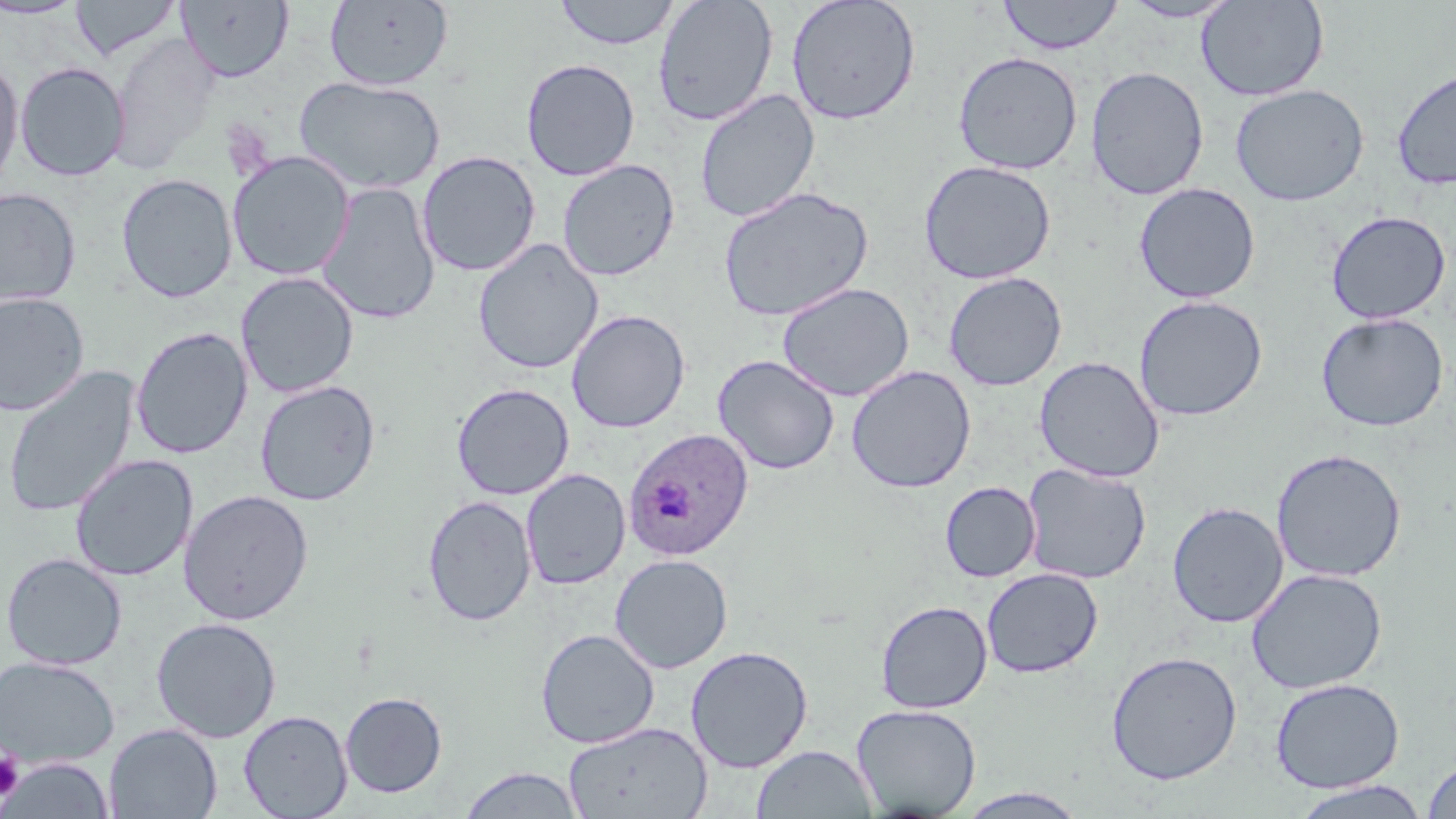

slide-level diagnosis = Plasmodium ovale
preparation = thin blood smear
magnification = 1000x
platelet locations = approximate bounding boxes as (x1,y1)-(x2,y2) corner pairs in pixels: (0,751)-(24,801)
field of view = one of a larger specimen
image size = 1456×819 pixels
modality = light microscopy
uninfected red blood cell locations = approximate bounding boxes as (x1,y1)-(x2,y2) corner pairs in pixels: (71,0)-(181,61), (324,0)-(454,91), (553,0)-(681,50), (652,0)-(779,127), (786,0)-(921,126), (996,0)-(1125,55), (1119,0)-(1241,23), (1196,0)-(1329,102), (0,1)-(87,19), (176,1)-(294,83), (108,34)-(221,173), (953,51)-(1083,175), (0,56)-(24,195), (520,58)-(640,182), (15,61)-(130,181), (1391,65)-(1456,190), (1085,66)-(1209,201), (293,76)-(446,195), (1229,83)-(1369,206), (695,89)-(820,224), (416,150)-(541,277), (227,151)-(355,281), (557,159)-(680,282), (918,160)-(1056,284), (116,173)-(237,304), (316,182)-(441,326), (1133,183)-(1261,304), (717,186)-(874,323), (0,188)-(81,307), (1325,211)-(1452,325), (472,238)-(604,375), (236,271)-(359,398), (943,271)-(1067,391), (777,282)-(915,402), (0,292)-(90,416), (1133,295)-(1268,421), (567,309)-(690,433), (1316,313)-(1448,432), (130,326)-(253,459), (712,354)-(840,475), (1034,356)-(1165,483), (2,366)-(140,519), (846,366)-(976,493), (255,380)-(380,506), (451,382)-(575,501), (1271,448)-(1407,582), (70,454)-(197,582), (1021,462)-(1152,584), (521,468)-(630,590), (939,481)-(1041,582), (178,489)-(315,626), (422,494)-(537,626), (1167,501)-(1288,628), (1,552)-(127,670), (609,553)-(734,674), (981,567)-(1104,678), (1246,567)-(1388,694), (875,600)-(992,713), (150,617)-(282,742), (535,628)-(659,748), (685,645)-(813,773), (1106,650)-(1243,785), (0,656)-(120,769), (1270,677)-(1404,793), (340,691)-(447,798), (851,703)-(982,817), (238,709)-(353,818), (562,721)-(712,819), (104,723)-(222,818), (751,744)-(878,818), (2,757)-(115,818), (1422,758)-(1456,818), (458,766)-(587,818), (1290,780)-(1430,818), (954,787)-(1091,818)
Plasmodium ovale-infected red blood cell locations = approximate bounding boxes as (x1,y1)-(x2,y2) corner pairs in pixels: (623,427)-(754,561)
stain = May-Grünwald-Giemsa